Report the malaria status of this cell.
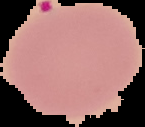

Parasitized.

Summary:
  - Preparation: thin blood smear
  - Image type: segmented cell region on a black background
  - Image size: 145×127 pixels